Assess this cell for malaria.
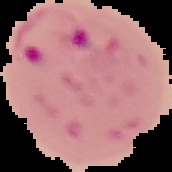
It is parasitized.

preparation: thin blood smear
image_type: segmented cell region with the area outside set to black
image_size: 172×172 pixels